Locate every blood parasite and identify its species.
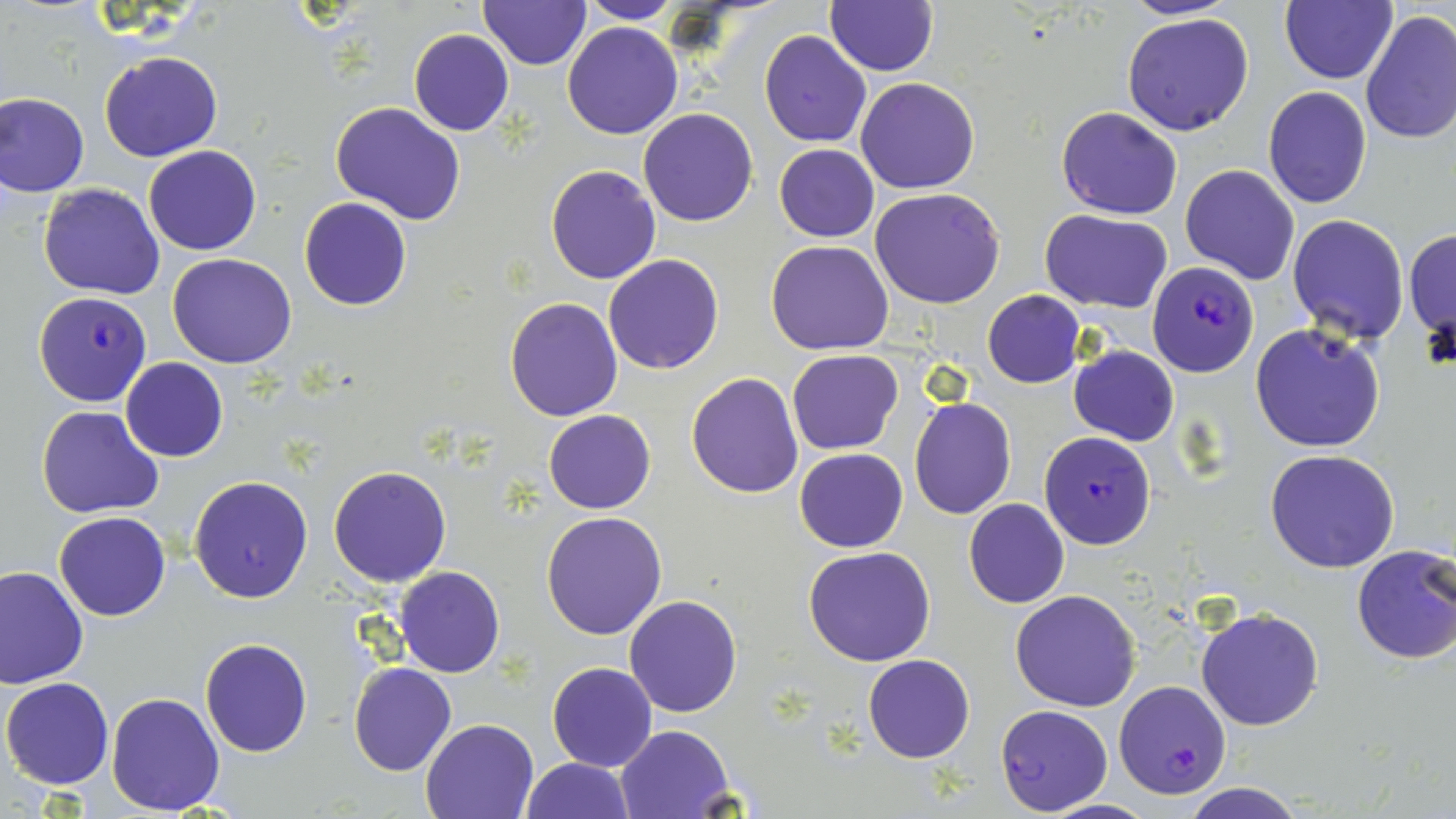

Approximate bounding boxes as (x1, y1, x2, y2) in pixels.
Plasmodium falciparum-infected red blood cells: (1148, 262, 1259, 378), (35, 291, 151, 407), (1038, 431, 1156, 549), (1113, 680, 1231, 800), (994, 704, 1112, 815).
No Plasmodium ovale, Plasmodium malariae, Plasmodium vivax, Babesia divergens, or Trypanosoma brucei observed.

slide-level diagnosis = Plasmodium falciparum
magnification = 1000x
field of view = single
uninfected red blood cell locations = approximate bounding boxes as (x1, y1, x2, y2) in pixels: (577, 0, 679, 24), (1116, 0, 1243, 19), (1281, 0, 1396, 83), (480, 1, 590, 69), (826, 1, 938, 76), (1360, 8, 1456, 145), (1122, 11, 1255, 136), (562, 21, 682, 141), (408, 29, 513, 137), (759, 30, 871, 146), (99, 51, 220, 161), (856, 77, 980, 193), (1264, 86, 1372, 209), (0, 93, 90, 197), (331, 102, 467, 224), (1057, 105, 1183, 219), (638, 109, 759, 227), (773, 144, 879, 241), (143, 146, 262, 255), (1180, 164, 1300, 284), (545, 165, 661, 284), (38, 184, 166, 299), (869, 188, 1007, 309), (299, 197, 412, 311), (1041, 210, 1172, 313), (1286, 214, 1410, 344), (1404, 227, 1455, 345), (766, 240, 894, 354), (168, 252, 296, 368), (603, 254, 724, 374), (983, 290, 1085, 387), (504, 297, 625, 422), (1250, 324, 1385, 451), (1070, 345, 1179, 446), (787, 349, 903, 453), (120, 358, 228, 462), (686, 372, 804, 498), (909, 397, 1017, 520), (37, 406, 165, 517), (544, 409, 655, 514), (794, 447, 908, 552), (1266, 448, 1400, 573), (329, 465, 452, 586), (188, 476, 313, 603), (964, 498, 1071, 609), (541, 512, 667, 639), (54, 513, 171, 621), (1351, 543, 1456, 665), (803, 546, 936, 666), (0, 564, 88, 688), (394, 567, 505, 678), (1010, 590, 1141, 712), (623, 595, 743, 717), (1196, 607, 1324, 731), (200, 637, 313, 757), (863, 653, 975, 763), (348, 662, 456, 776), (547, 662, 657, 772), (1, 677, 114, 790), (106, 690, 226, 816), (421, 717, 541, 819), (614, 725, 736, 819), (522, 758, 634, 818), (1181, 785, 1304, 819)
preparation = thin blood film
stain = May-Grünwald-Giemsa
image size = 1456×819 pixels
modality = light microscopy